Classify this cell by malaria status.
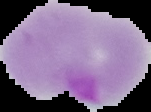
It is parasitized.

Segmented cell region on a black background. From a thin blood film. Image is 151×112 pixels.